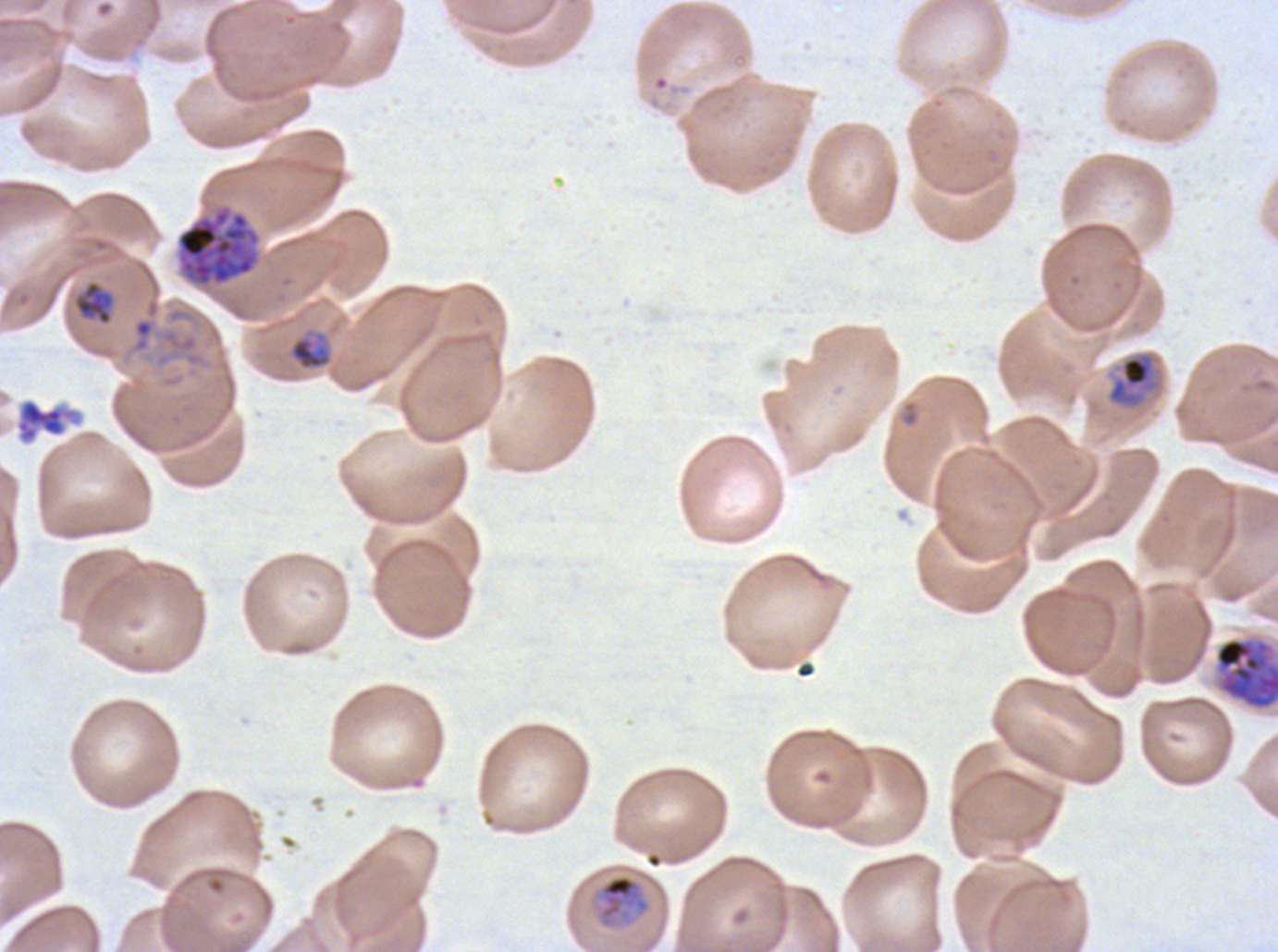
Approximate bounding boxes as (x1, y1, x2, y2) in pixels. Mid trophozoite locations: (1106, 350, 1163, 410), (593, 873, 652, 930). Late-ring/early-trophozoite locations: (73, 280, 115, 325), (288, 329, 333, 372). Late schizont locations: (176, 206, 260, 287). Early schizont locations: (1214, 637, 1277, 711). Debris locations: (14, 397, 84, 445). Image is 1278×952 pixels. Plasmodium falciparum from a patient in The Gambia, cultured ex vivo for 24 to 48 hours. Thin blood smear. Life-cycle stages observed: late-ring/early-trophozoite, mid trophozoite, early schizont, late schizont. One sub-image of a larger composite. Giemsa stain.